Assess the morphology of the erythrocytes.
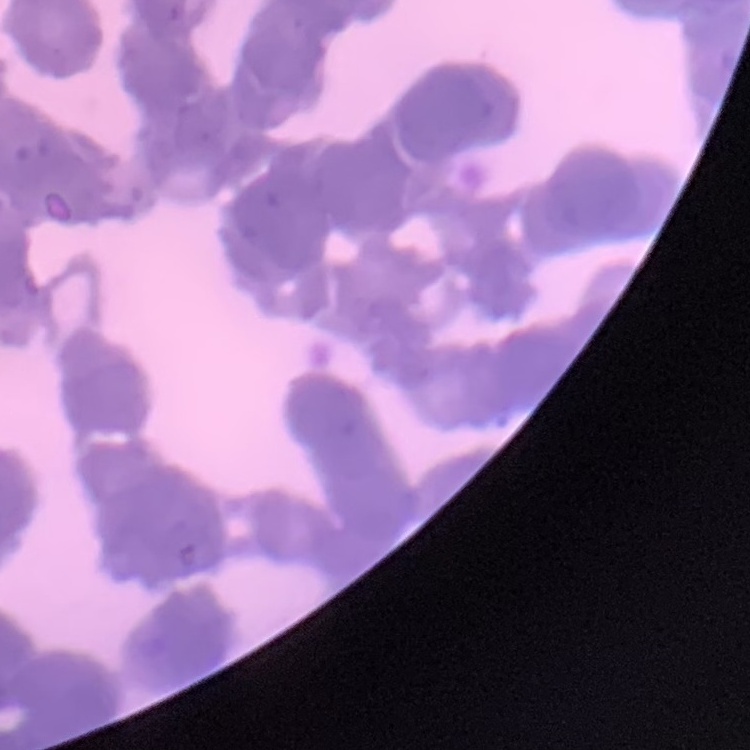

Rouleaux formation.

Summary:
  - Image type: one tile cut from a larger photomicrograph
  - Preparation: thin peripheral smear
  - Stain: Field's or Giemsa